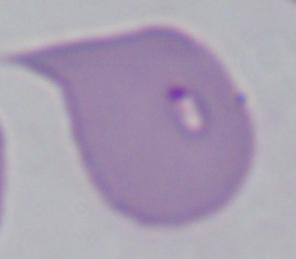

identification = Babesia
modality = micrograph
magnification = 1000x